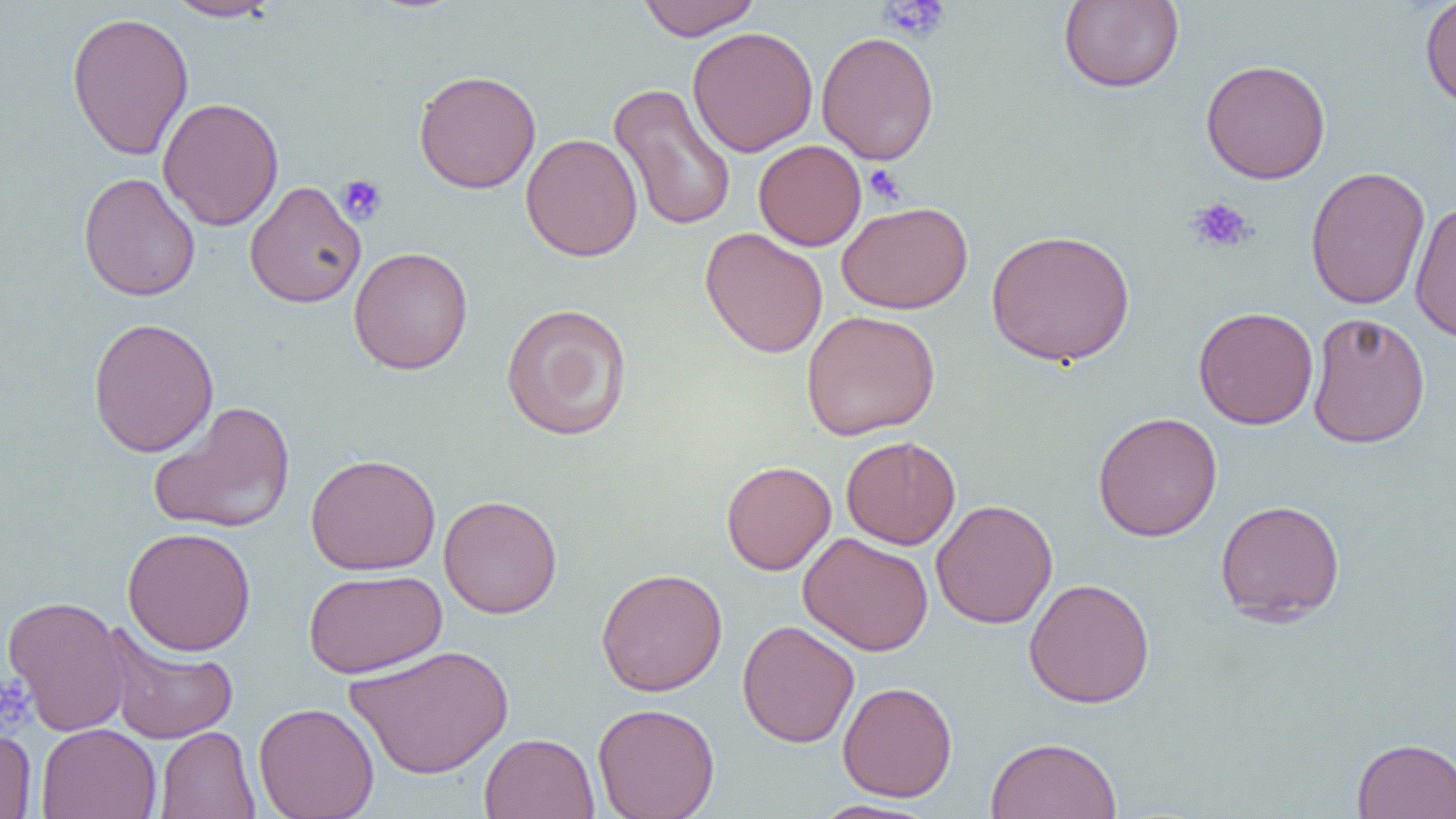

slide-level diagnosis = no evidence of blood parasites
platelet locations = approximate bounding boxes as named x1/y1/x2/y2 corners in pixels: (x1=880, y1=0, x2=951, y2=42), (x1=863, y1=163, x2=906, y2=206), (x1=335, y1=174, x2=388, y2=226), (x1=1186, y1=197, x2=1255, y2=254), (x1=0, y1=671, x2=37, y2=736)
preparation = thin blood film
magnification = 1000x
image size = 1456×819 pixels
uninfected red blood cell locations = approximate bounding boxes as named x1/y1/x2/y2 corners in pixels: (x1=164, y1=0, x2=283, y2=22), (x1=636, y1=0, x2=762, y2=41), (x1=1058, y1=0, x2=1184, y2=92), (x1=1419, y1=0, x2=1456, y2=110), (x1=66, y1=11, x2=194, y2=161), (x1=687, y1=26, x2=819, y2=158), (x1=816, y1=31, x2=939, y2=165), (x1=1200, y1=59, x2=1331, y2=184), (x1=413, y1=69, x2=541, y2=194), (x1=608, y1=83, x2=737, y2=232), (x1=157, y1=97, x2=285, y2=232), (x1=521, y1=133, x2=643, y2=262), (x1=753, y1=140, x2=867, y2=251), (x1=1304, y1=165, x2=1431, y2=311), (x1=78, y1=172, x2=200, y2=302), (x1=244, y1=180, x2=366, y2=309), (x1=1409, y1=200, x2=1456, y2=342), (x1=836, y1=201, x2=974, y2=315), (x1=699, y1=227, x2=828, y2=359), (x1=986, y1=229, x2=1135, y2=367), (x1=348, y1=246, x2=473, y2=375), (x1=500, y1=302, x2=633, y2=441), (x1=1193, y1=306, x2=1319, y2=430), (x1=801, y1=309, x2=941, y2=441), (x1=1306, y1=313, x2=1431, y2=449), (x1=87, y1=316, x2=219, y2=457), (x1=148, y1=400, x2=296, y2=534), (x1=1093, y1=411, x2=1222, y2=541), (x1=841, y1=435, x2=961, y2=550), (x1=304, y1=452, x2=441, y2=576), (x1=721, y1=460, x2=836, y2=575), (x1=438, y1=495, x2=562, y2=618), (x1=931, y1=499, x2=1058, y2=629), (x1=1215, y1=499, x2=1346, y2=625), (x1=122, y1=526, x2=256, y2=656), (x1=797, y1=532, x2=934, y2=656), (x1=596, y1=567, x2=728, y2=696), (x1=304, y1=568, x2=447, y2=678), (x1=1024, y1=578, x2=1155, y2=708), (x1=2, y1=594, x2=130, y2=737), (x1=737, y1=620, x2=859, y2=747), (x1=102, y1=623, x2=239, y2=744), (x1=345, y1=645, x2=515, y2=779), (x1=837, y1=681, x2=958, y2=802), (x1=253, y1=702, x2=380, y2=819), (x1=593, y1=702, x2=720, y2=819), (x1=36, y1=723, x2=161, y2=819), (x1=0, y1=725, x2=37, y2=818), (x1=155, y1=726, x2=260, y2=819), (x1=479, y1=732, x2=599, y2=819), (x1=985, y1=736, x2=1122, y2=819), (x1=1351, y1=737, x2=1456, y2=818), (x1=810, y1=799, x2=939, y2=819)
modality = optical microscopy
field of view = one of a larger specimen